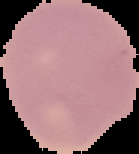

Summary:
  - Preparation: thin blood film
  - Result: no Plasmodium parasites seen
  - Image type: segmented cell region with the area outside set to black
  - Image size: 139×154 pixels